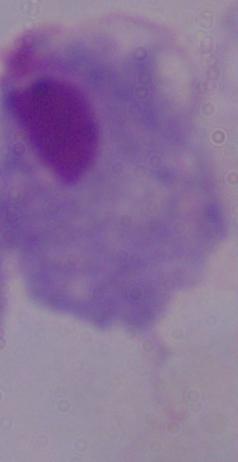
Summary:
  - Modality: photomicrograph
  - Magnification: 1000x
  - Identification: trichomonad